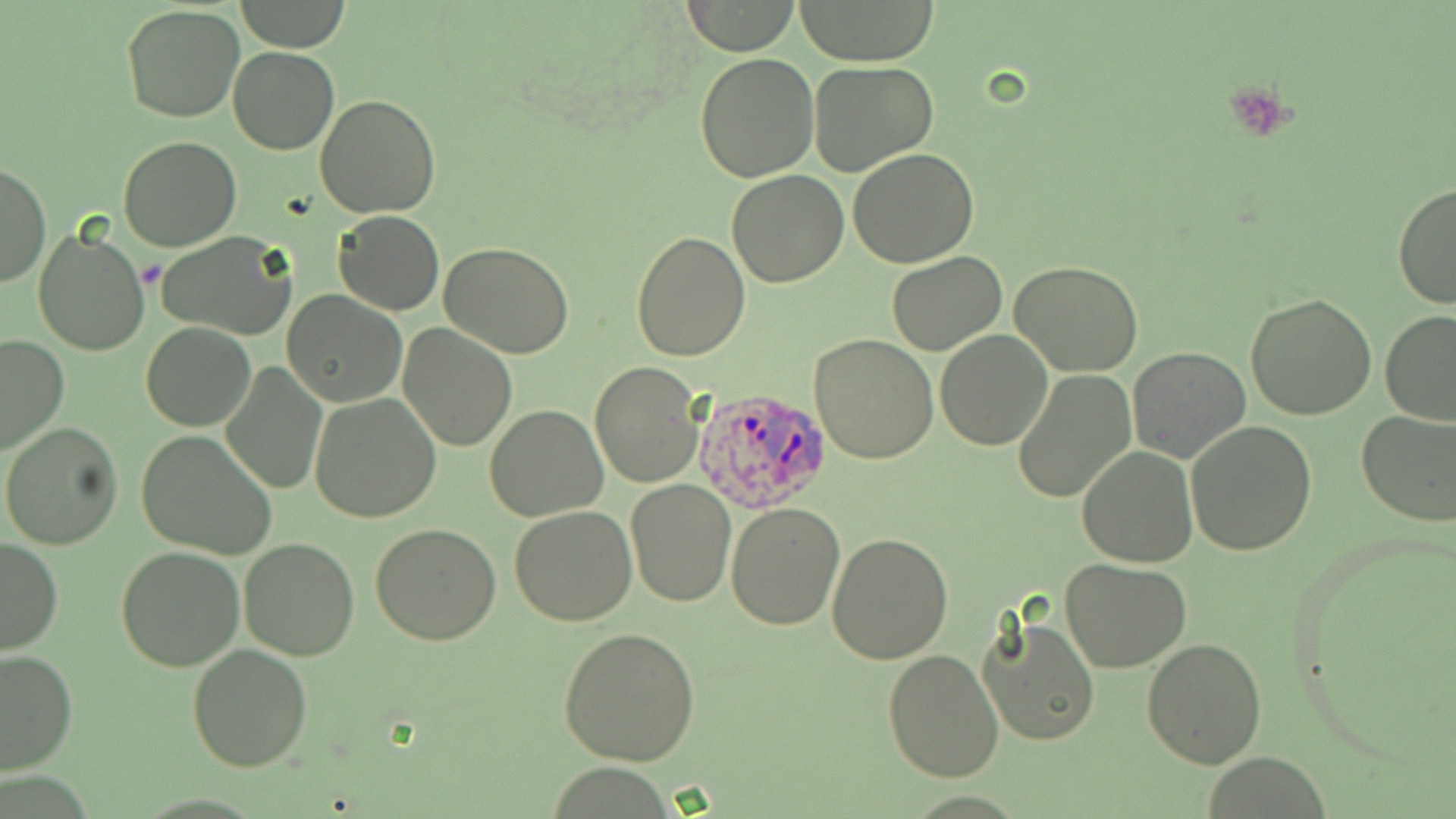
Summary:
  - Coordinate format: approximate bounding boxes as (x1,y1)-(x2,y2) corner pairs in pixels
  - Plasmodium ovale-infected red blood cell locations: (692,386)-(835,514)
  - Platelet locations: (1225,78)-(1303,142)
  - Uninfected red blood cell locations: (681,0)-(802,55), (793,0)-(940,65), (235,1)-(349,52), (120,4)-(245,123), (228,47)-(340,154), (694,51)-(820,183), (808,60)-(938,176), (314,94)-(442,218), (117,135)-(242,252), (847,147)-(978,267), (1,161)-(50,289), (726,170)-(849,287), (1394,181)-(1456,311), (332,210)-(444,315), (33,224)-(153,357), (629,230)-(750,360), (153,231)-(300,342), (439,242)-(574,358), (885,251)-(1009,355), (1009,260)-(1144,377), (282,291)-(408,407), (1244,293)-(1377,420), (1379,309)-(1456,426), (140,322)-(255,431), (397,323)-(520,450), (935,328)-(1052,449), (809,334)-(939,464), (0,335)-(69,455), (1127,347)-(1251,463), (591,360)-(705,486), (220,363)-(327,494), (1013,367)-(1138,504), (311,394)-(442,522), (484,404)-(608,521), (1356,408)-(1456,526), (1186,418)-(1316,555), (1,422)-(124,552), (136,430)-(278,560), (1077,447)-(1197,566), (625,479)-(737,607), (726,501)-(847,630), (509,506)-(639,625), (369,524)-(500,645), (825,532)-(954,665), (0,538)-(63,655), (238,538)-(360,661), (115,546)-(245,671), (1060,558)-(1191,672), (978,613)-(1100,747), (557,625)-(700,766), (1141,637)-(1268,769), (186,644)-(312,772), (882,648)-(1005,782), (0,649)-(76,775)
  - Slide-level diagnosis: Plasmodium ovale
  - Preparation: thin blood film
  - Image size: 1456×819 pixels
  - Magnification: 1000x
  - Field of view: single
  - Stain: May-Grünwald-Giemsa
  - Modality: light microscopy